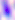 Photomicrograph. Toxoplasma gondii is shown. 400x magnification.